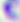
magnification: 400x
identification: Toxoplasma gondii
modality: micrograph